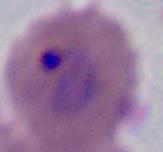

Photomicrograph. Captured at either 400x or 1000x magnification. A Plasmodium parasite is shown.